Report the malaria status of this cell.
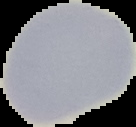
Uninfected.

Summary:
  - Image type: segmented cell region with the area outside set to black
  - Image size: 136×127 pixels
  - Preparation: thin blood smear